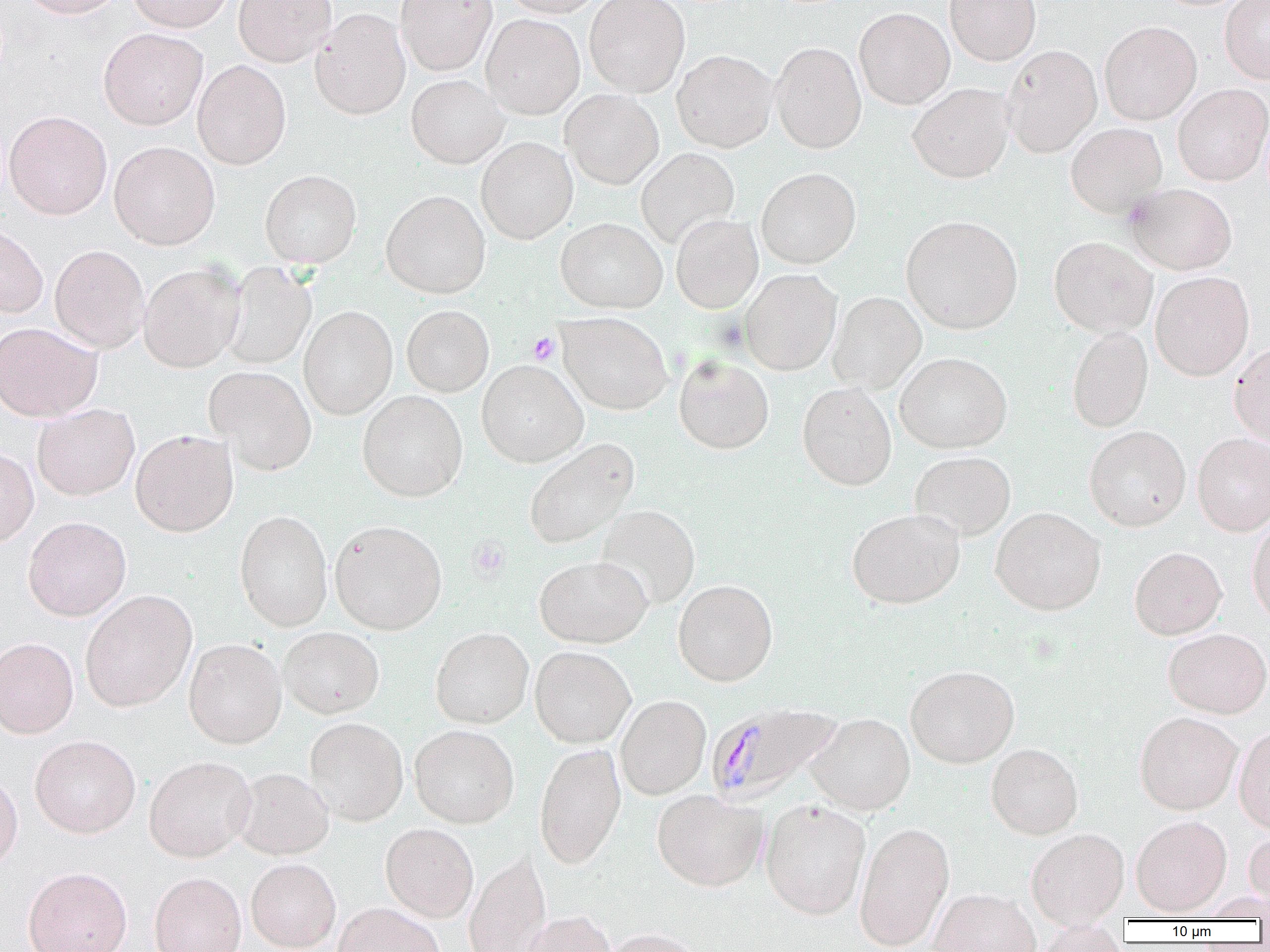 Approximate bounding boxes as [x1, y1, x2, y2] in pixels. Platelet locations: [527, 332, 559, 365], [468, 537, 510, 581]. Uninfected red blood cell locations: [18, 0, 128, 19], [127, 0, 235, 32], [233, 0, 336, 66], [395, 0, 497, 76], [500, 0, 606, 18], [584, 0, 690, 98], [945, 0, 1041, 65], [1220, 0, 1270, 83], [853, 7, 955, 109], [310, 8, 411, 120], [481, 13, 585, 119], [1099, 21, 1202, 125], [98, 28, 208, 130], [770, 41, 867, 154], [1001, 44, 1102, 158], [672, 50, 778, 152], [192, 60, 291, 169], [406, 74, 509, 168], [908, 83, 1014, 183], [1172, 84, 1270, 186], [561, 90, 664, 189], [3, 110, 112, 220], [1066, 122, 1168, 217], [476, 137, 578, 244], [109, 141, 220, 250], [636, 147, 739, 248], [756, 167, 861, 269], [260, 169, 362, 268], [1125, 183, 1237, 274], [381, 190, 491, 298], [671, 214, 763, 314], [901, 215, 1023, 334], [555, 217, 667, 313], [0, 225, 48, 318], [1049, 236, 1158, 336], [49, 245, 149, 353], [138, 263, 244, 372], [220, 263, 317, 369], [739, 268, 841, 375], [1150, 271, 1254, 380], [828, 291, 926, 394], [402, 305, 494, 396], [299, 306, 397, 419], [557, 312, 673, 415], [0, 322, 101, 421], [1067, 325, 1153, 433], [1229, 342, 1270, 447], [895, 352, 1012, 453], [674, 355, 774, 454], [477, 360, 588, 466], [204, 365, 317, 475], [798, 382, 897, 490], [358, 391, 467, 501], [32, 403, 139, 500], [1084, 425, 1191, 531], [130, 429, 238, 537], [1192, 433, 1270, 535], [523, 438, 639, 550], [0, 448, 39, 547], [910, 451, 1016, 541], [595, 504, 700, 611], [991, 507, 1106, 615], [847, 509, 965, 609], [235, 510, 333, 631], [23, 516, 131, 621], [1247, 517, 1270, 626], [329, 519, 447, 634], [1129, 546, 1227, 639], [534, 555, 652, 648], [673, 580, 778, 686], [80, 590, 198, 712], [279, 627, 385, 718], [430, 627, 533, 729], [1163, 628, 1270, 718], [184, 634, 383, 729], [0, 637, 79, 738], [183, 638, 287, 748], [530, 646, 636, 748], [905, 665, 1020, 767], [616, 695, 711, 800], [1135, 712, 1242, 814], [807, 713, 915, 815], [305, 717, 408, 825], [1234, 724, 1270, 835], [409, 725, 519, 828], [29, 735, 141, 838], [534, 743, 626, 869], [986, 743, 1083, 839], [144, 756, 256, 862], [232, 768, 334, 859], [0, 772, 23, 874], [652, 789, 767, 891], [760, 799, 871, 919], [1131, 815, 1231, 916], [854, 821, 955, 951], [380, 823, 478, 922], [1026, 828, 1128, 927], [1244, 828, 1270, 914], [464, 851, 551, 952], [246, 858, 342, 952], [23, 866, 132, 952], [149, 872, 246, 952], [929, 888, 1040, 952], [334, 902, 443, 952], [521, 910, 616, 952], [1033, 922, 1128, 952], [600, 928, 704, 952]. Plasmodium malariae-infected red blood cell locations: [706, 702, 844, 805]. Slide-level diagnosis: Plasmodium malariae. Captured at 1000x magnification. Thin blood film. Light microscopy. Single field of view. Image is 1270×952 pixels.